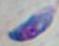
modality = micrograph
identification = Toxoplasma gondii
magnification = 1000x